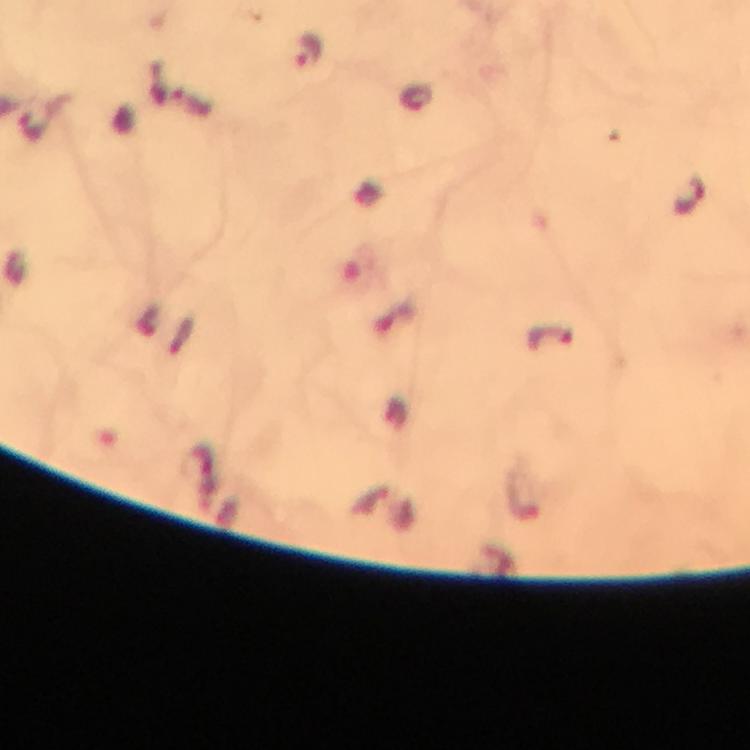
Approximate object centers, in pixels from the top-left corner.
Summary:
  - Plasmodium parasite locations: (x=310, y=49), (x=416, y=97), (x=691, y=196), (x=551, y=336)
  - Preparation: thick blood film
  - Immersion oil: applied
  - Cropped from: a single field of view
  - Stain: Giemsa
  - Capture: smartphone camera through the microscope
  - Magnification: 100x
  - Context: from a malaria diagnostic workup
  - Image size: 750×750 pixels